State the blood parasite species.
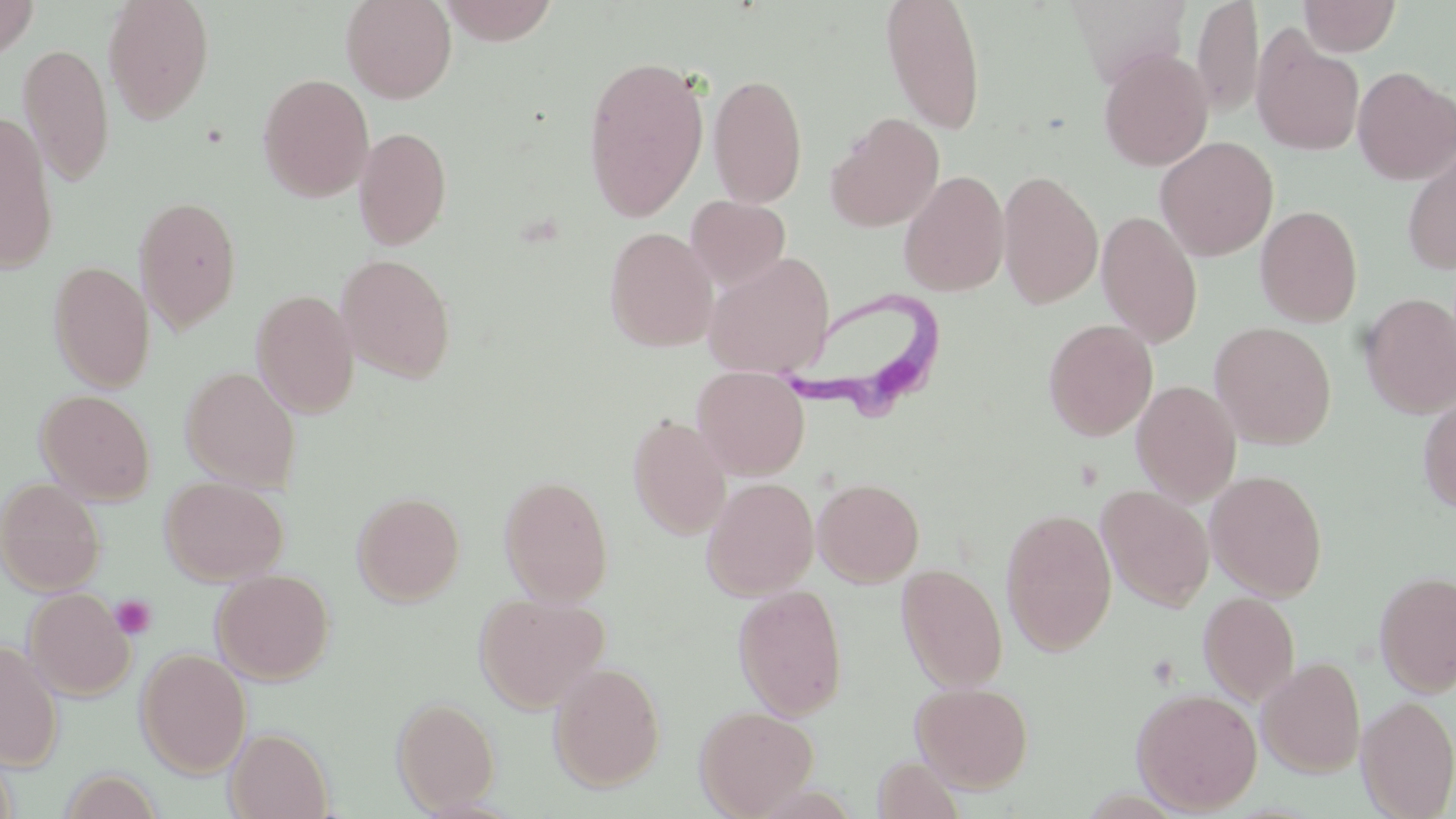
Trypanosoma brucei.

Summary:
  - Coordinate format: approximate bounding boxes as (x1,y1)-(x2,y2) corner pairs in pixels
  - Uninfected red blood cell locations: (0,0)-(39,59), (102,0)-(215,124), (340,0)-(457,104), (437,0)-(561,45), (879,0)-(988,136), (1067,0)-(1191,87), (1191,0)-(1264,119), (1298,0)-(1402,56), (1250,27)-(1365,157), (18,44)-(115,187), (1098,49)-(1214,171), (583,54)-(710,223), (1352,66)-(1456,185), (257,73)-(374,202), (708,73)-(808,207), (0,112)-(59,274), (826,112)-(944,232), (353,126)-(452,251), (1155,136)-(1278,261), (1401,143)-(1456,276), (898,170)-(1009,297), (997,171)-(1103,309), (133,195)-(243,335), (686,195)-(791,289), (1255,205)-(1363,327), (1096,211)-(1202,347), (604,226)-(718,352), (702,252)-(836,378), (335,253)-(457,383), (48,261)-(155,392), (250,289)-(360,418), (1359,293)-(1456,418), (1043,319)-(1158,440), (1210,321)-(1337,449), (180,366)-(301,490), (692,366)-(810,479), (1132,379)-(1242,505), (36,389)-(156,504), (1417,394)-(1456,514), (628,415)-(731,540), (1205,469)-(1328,601), (498,474)-(614,605), (160,475)-(288,585), (701,476)-(820,600), (0,477)-(106,596), (813,477)-(924,586), (1097,485)-(1214,612), (352,490)-(466,606), (1001,508)-(1118,655), (897,564)-(1008,692), (211,569)-(335,685), (1374,569)-(1456,697), (733,584)-(848,720), (23,587)-(135,701), (474,592)-(609,713), (1198,592)-(1300,706), (0,639)-(63,770), (136,647)-(251,778), (1257,656)-(1367,777), (548,660)-(666,792), (911,681)-(1034,792), (1131,687)-(1264,814), (1357,695)-(1456,818), (392,696)-(501,813), (695,705)-(819,818), (225,727)-(334,819), (872,756)-(967,818), (58,769)-(163,818)
  - Trypanosoma brucei locations: (774,282)-(950,414)
  - Platelet locations: (110,595)-(157,640)
  - Preparation: thin blood smear
  - Modality: optical microscopy
  - Stain: May-Grünwald-Giemsa
  - Field of view: one of a larger specimen
  - Image size: 1456×819 pixels
  - Magnification: 1000x